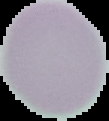
image type = segmented cell region with the area outside set to black
image size = 109×121 pixels
preparation = thin blood smear
result = no Plasmodium parasites seen